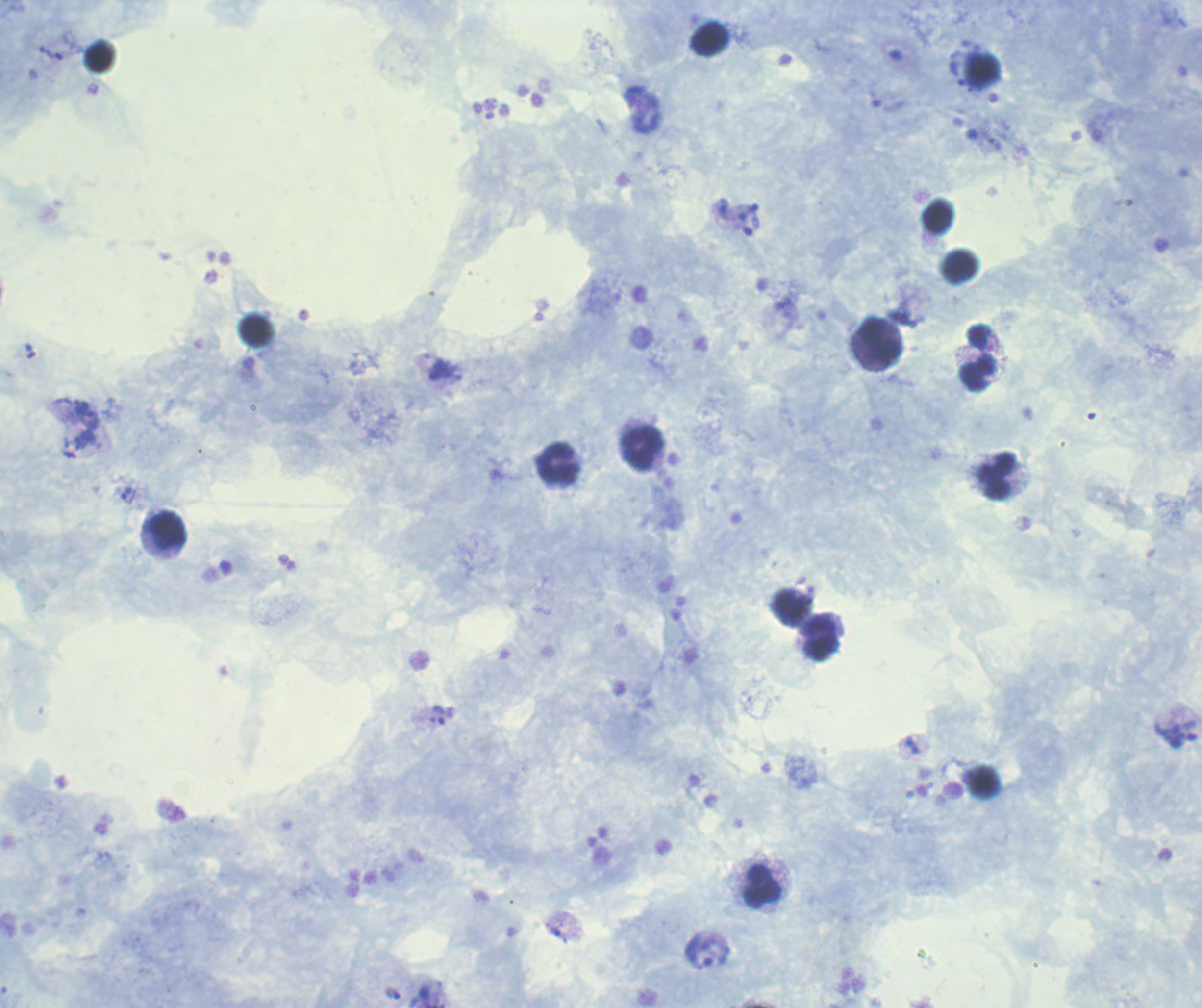
Approximate centers as [x, y] in pixels.
Summary:
  - Trophozoite locations: [45, 52], [957, 72], [80, 407], [91, 420], [126, 492], [439, 715], [555, 929], [700, 953], [393, 993]
  - Leukocyte locations: [709, 41], [880, 341], [978, 358], [642, 449], [557, 464], [997, 477], [166, 530], [821, 637], [763, 886]
  - Background quality: satisfactory
  - Preparation: thick smear of blood
  - Magnification: 100x
  - Field of view: single
  - Image size: 1202×1008 pixels
  - Context: previously used in an actual diagnosis
  - Stain: Romanowsky
  - Result: positive for Plasmodium parasites
  - Coloration quality: good